Comment on the morphology of the erythrocytes.
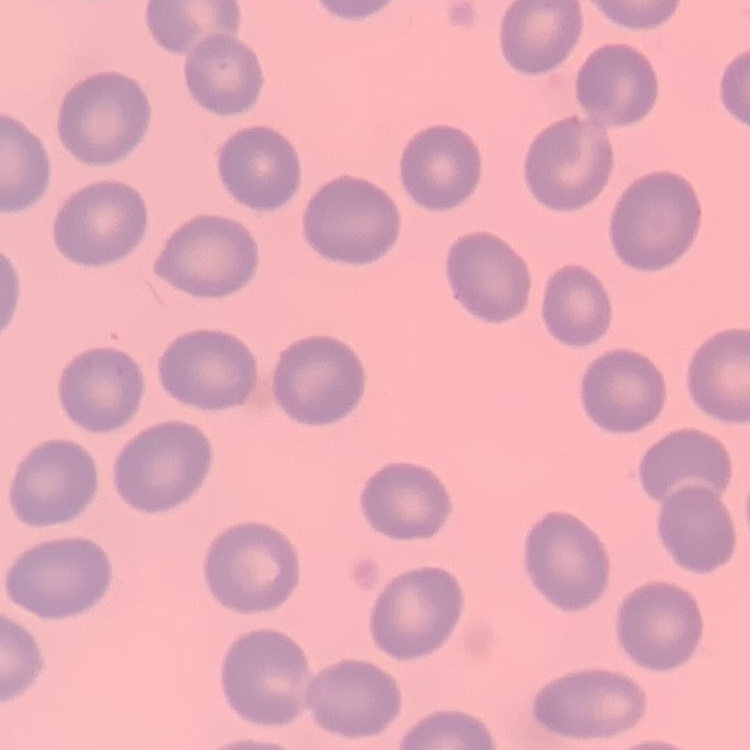
They show no rouleaux formation.

Square crop of a larger photomicrograph. Thin blood smear. Stained with either Field's or Giemsa.